Evaluate for Plasmodium parasites.
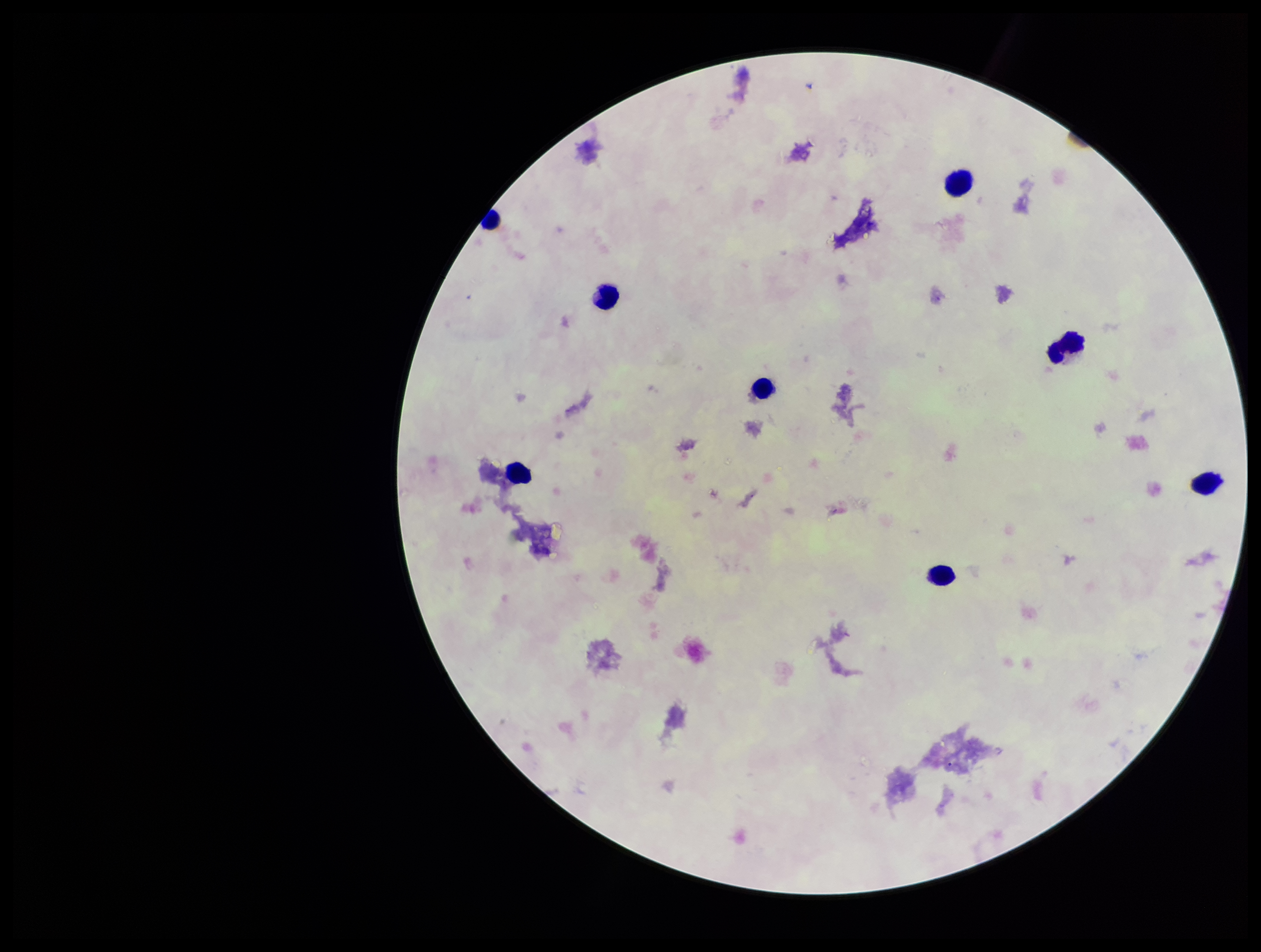

None seen.

Summary:
  - Parasite count: 0
  - Image size: 1261×952 pixels
  - Stain: Giemsa
  - Leukocyte count: 8
  - Capture: smartphone photograph through the microscope eyepiece
  - Preparation: thick smear
  - Patient malaria status: negative
  - Field of view: one from this slide